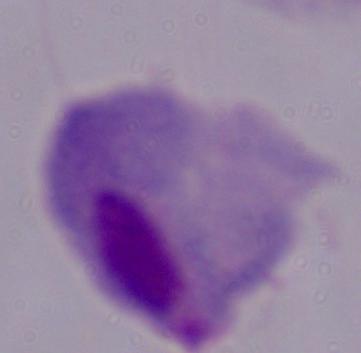

Summary:
  - Magnification: 1000x
  - Identification: trichomonad
  - Modality: micrograph